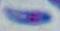

magnification = 1000x
identification = Toxoplasma gondii
modality = micrograph